Comment on the morphology of the erythrocytes.
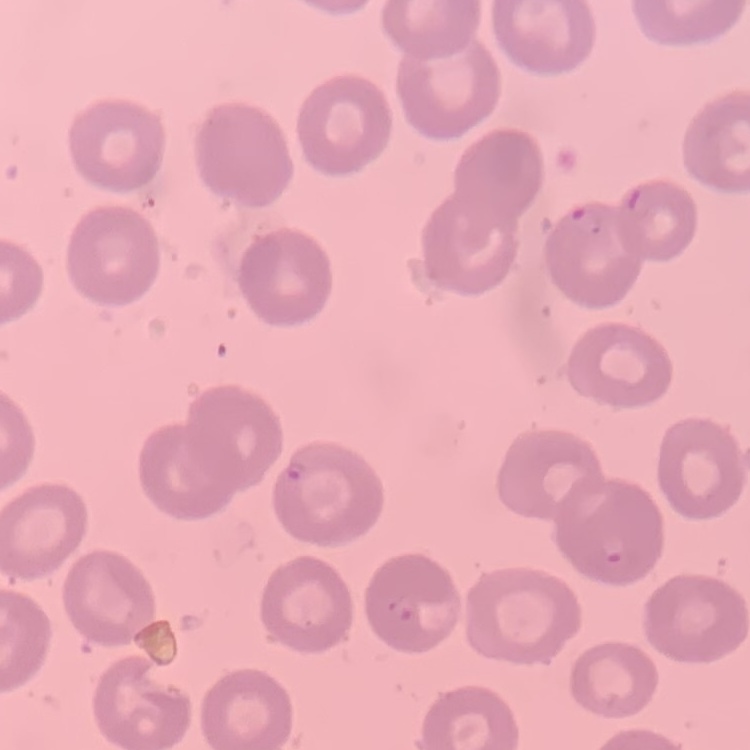
No rouleaux formation.

Summary:
  - Image type: one tile cut from a larger photomicrograph
  - Stain: Field's or Giemsa
  - Preparation: thin blood smear